State which cell type is depicted.
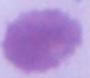

An erythrocyte.

Captured at 1000x magnification. Photomicrograph.